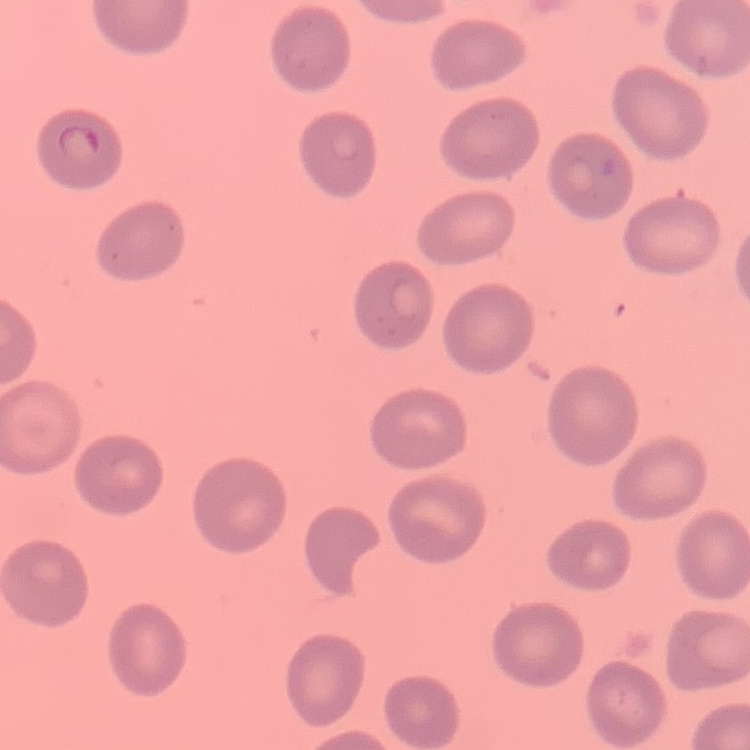

erythrocyte morphology = no rouleaux formation
preparation = thin blood smear
stain = Field's or Giemsa
image type = square crop of a larger photomicrograph